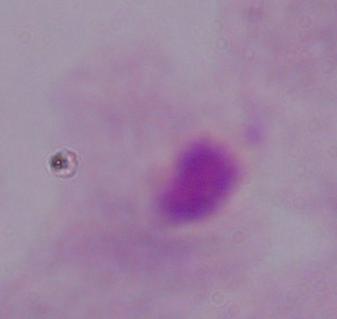
Summary:
  - Magnification: 1000x
  - Modality: micrograph
  - Identification: trichomonad